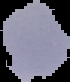
Summary:
  - Result: negative for malaria parasites
  - Image size: 70×82 pixels
  - Preparation: thin blood film
  - Image type: segmented cell region with the area outside set to black